Locate and identify every blood parasite.
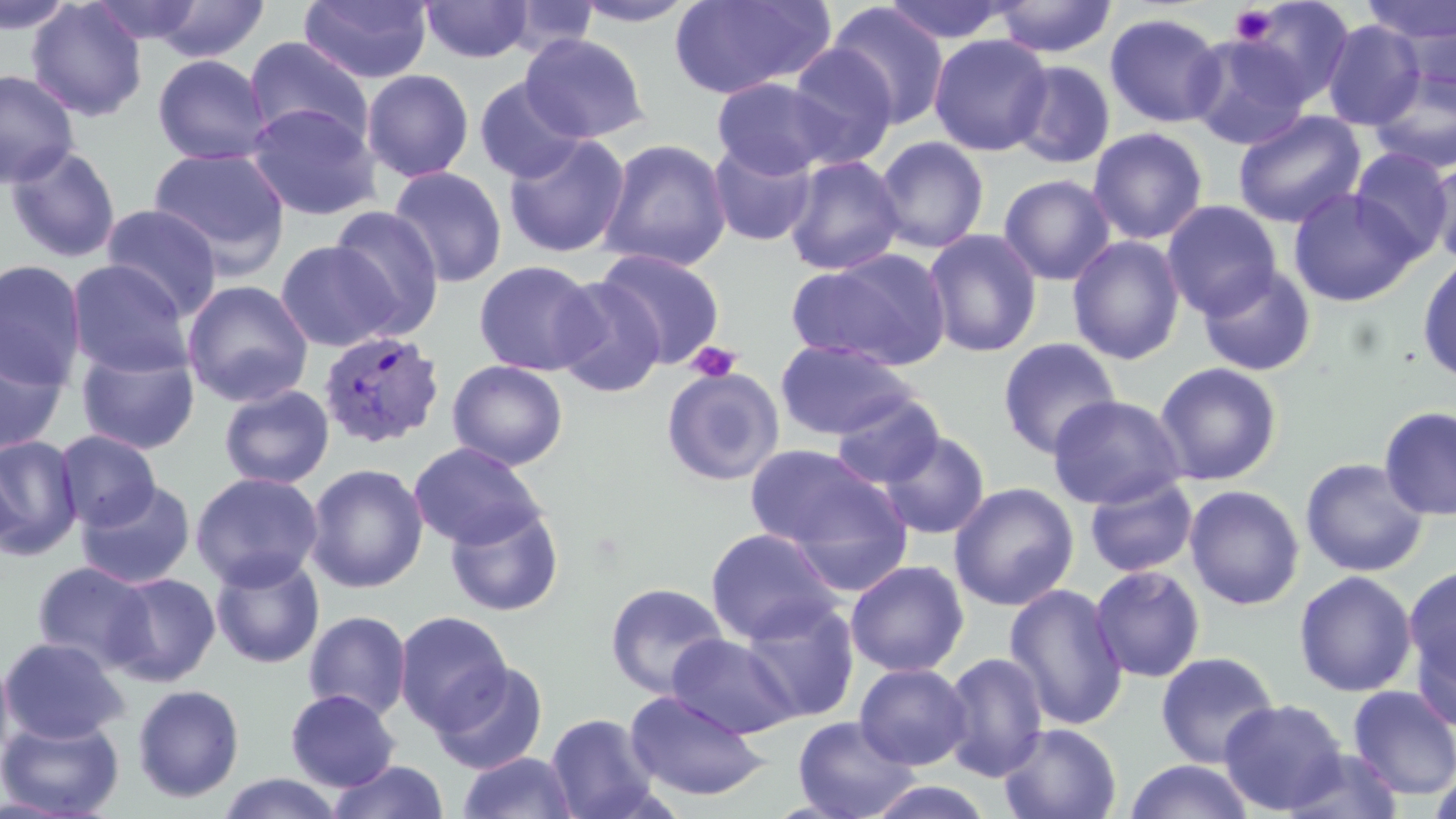

Approximate bounding boxes as (x1, y1, x2, y2) in pixels.
Plasmodium vivax-infected red blood cells: (317, 330, 446, 450).
No Plasmodium falciparum, Plasmodium ovale, Plasmodium malariae, Babesia divergens, or Trypanosoma brucei observed.

Summary:
  - Platelet locations: (1230, 5, 1277, 46), (686, 341, 742, 383)
  - Uninfected red blood cell locations: (0, 0, 77, 36), (89, 0, 205, 45), (151, 0, 271, 63), (298, 0, 433, 84), (569, 0, 701, 28), (669, 0, 834, 99), (881, 0, 1013, 44), (992, 0, 1117, 58), (1235, 0, 1356, 107), (26, 1, 148, 121), (420, 1, 534, 64), (1360, 1, 1456, 47), (826, 3, 950, 128), (1104, 12, 1227, 129), (1393, 16, 1456, 107), (1321, 20, 1426, 130), (519, 33, 649, 143), (928, 34, 1052, 157), (1186, 34, 1312, 151), (244, 36, 374, 149), (784, 43, 899, 169), (152, 54, 272, 166), (1009, 60, 1116, 169), (0, 68, 80, 189), (1367, 68, 1456, 175), (361, 69, 474, 182), (711, 77, 840, 179), (474, 78, 587, 184), (244, 102, 382, 222), (1232, 110, 1366, 229), (1087, 127, 1208, 245), (502, 133, 631, 258), (873, 136, 989, 254), (598, 138, 732, 271), (707, 139, 819, 247), (4, 145, 122, 264), (148, 146, 291, 275), (1348, 147, 1454, 259), (783, 154, 905, 276), (1427, 158, 1456, 267), (387, 166, 508, 289), (999, 174, 1116, 285), (1288, 188, 1420, 306), (1161, 199, 1282, 319), (100, 204, 223, 319), (328, 205, 445, 338), (923, 229, 1043, 358), (1067, 234, 1186, 365), (275, 240, 399, 352), (595, 247, 725, 367), (786, 249, 952, 371), (1417, 255, 1456, 384), (0, 260, 87, 389), (65, 260, 194, 378), (473, 260, 601, 376), (1197, 264, 1317, 378), (551, 276, 666, 397), (181, 279, 314, 407), (0, 333, 68, 456), (997, 337, 1122, 458), (775, 338, 918, 440), (75, 344, 200, 455), (447, 359, 568, 470), (1153, 361, 1283, 486), (661, 366, 784, 486), (218, 384, 335, 490), (831, 393, 945, 489), (1047, 394, 1187, 509), (1378, 405, 1456, 521), (54, 430, 161, 531), (878, 430, 990, 539), (0, 435, 83, 560), (408, 442, 546, 549), (744, 444, 898, 556), (1300, 457, 1430, 578), (305, 463, 429, 594), (190, 472, 323, 590), (1084, 474, 1198, 578), (76, 480, 196, 589), (948, 482, 1079, 611), (1184, 484, 1305, 610), (444, 503, 565, 617), (705, 528, 842, 644), (210, 553, 325, 669), (845, 559, 969, 676), (32, 561, 154, 671), (1404, 564, 1456, 690), (1089, 565, 1206, 683), (1294, 570, 1418, 697), (104, 572, 221, 686), (605, 582, 729, 698), (1004, 583, 1128, 731), (739, 598, 861, 723), (303, 610, 412, 722), (394, 610, 512, 731), (1410, 619, 1456, 734), (667, 634, 800, 738), (0, 636, 129, 744), (0, 649, 14, 773), (940, 651, 1050, 782), (1155, 651, 1280, 768), (431, 661, 549, 774), (854, 662, 973, 770), (132, 683, 245, 803), (1347, 685, 1456, 799), (285, 689, 400, 792), (624, 691, 770, 802), (1219, 698, 1348, 814), (545, 712, 661, 818), (0, 715, 125, 818), (792, 716, 919, 819), (998, 722, 1122, 819), (1281, 747, 1406, 818), (456, 751, 580, 819), (1123, 759, 1255, 819), (327, 760, 450, 819), (216, 773, 346, 818), (864, 780, 996, 819)
  - Slide-level diagnosis: Plasmodium vivax
  - Preparation: thin blood film
  - Image size: 1456×819 pixels
  - Magnification: 1000x
  - Stain: May-Grünwald-Giemsa
  - Modality: light microscopy
  - Field of view: single